Locate every blood parasite and identify its species.
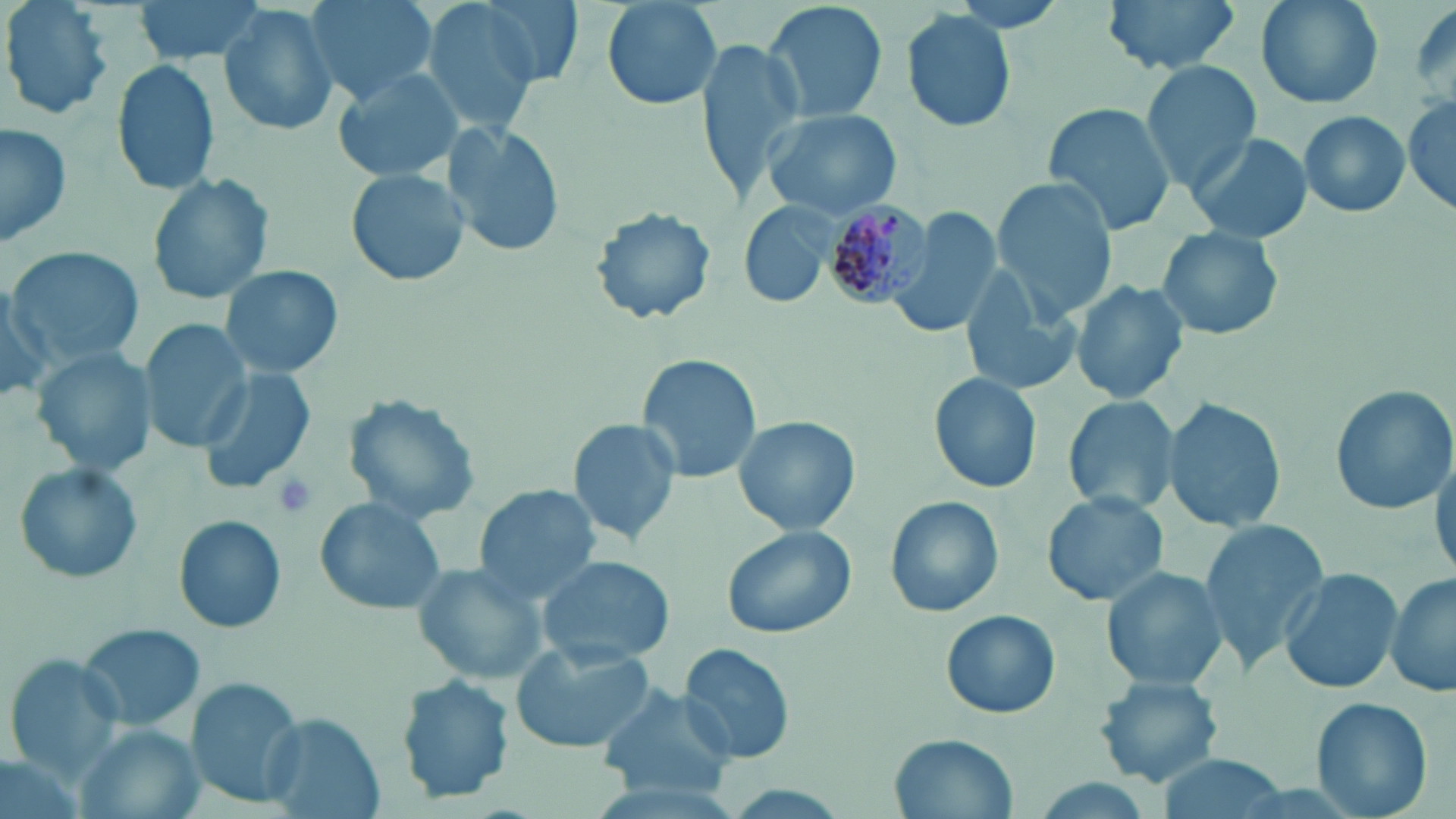

Approximate bounding boxes as [x1, y1, x2, y2] in pixels.
Plasmodium malariae-infected red blood cells: [818, 198, 933, 308].
No Plasmodium falciparum, Plasmodium ovale, Plasmodium vivax, Babesia divergens, or Trypanosoma brucei observed.

Uninfected red blood cell locations: [2, 0, 112, 125], [136, 0, 267, 65], [305, 0, 440, 105], [420, 0, 557, 134], [471, 0, 586, 89], [599, 0, 724, 111], [763, 0, 887, 126], [1102, 0, 1243, 76], [1251, 0, 1385, 112], [218, 6, 341, 138], [902, 12, 1017, 132], [695, 36, 805, 201], [1140, 60, 1264, 190], [112, 61, 220, 194], [332, 69, 465, 185], [1402, 94, 1455, 221], [1044, 100, 1178, 237], [1296, 109, 1412, 218], [764, 110, 900, 218], [442, 121, 566, 258], [0, 122, 75, 249], [1187, 131, 1314, 243], [345, 168, 470, 289], [147, 171, 274, 306], [992, 176, 1118, 321], [737, 201, 838, 310], [588, 203, 719, 327], [885, 209, 1002, 339], [1157, 226, 1286, 340], [3, 244, 147, 368], [220, 264, 341, 379], [959, 270, 1083, 400], [0, 279, 52, 405], [1070, 283, 1188, 405], [141, 320, 252, 450], [33, 347, 156, 477], [639, 354, 766, 485], [198, 364, 319, 493], [929, 373, 1043, 495], [1329, 383, 1454, 514], [342, 393, 483, 520], [1062, 395, 1181, 516], [1162, 395, 1289, 536], [731, 414, 860, 535], [569, 418, 682, 546], [1431, 444, 1455, 582], [11, 461, 146, 587], [473, 484, 600, 604], [1042, 491, 1169, 607], [884, 494, 1005, 619], [313, 497, 447, 614], [172, 514, 288, 634], [1199, 517, 1331, 670], [722, 524, 859, 638], [538, 557, 677, 663], [410, 560, 548, 685], [1101, 565, 1229, 692], [1279, 566, 1401, 694], [1386, 573, 1454, 700], [941, 611, 1061, 720], [78, 621, 206, 732], [509, 641, 656, 755], [678, 641, 798, 764], [3, 656, 123, 778], [1093, 672, 1225, 788], [398, 676, 514, 803], [185, 679, 307, 806], [598, 687, 732, 799], [1311, 697, 1432, 818], [258, 713, 383, 817], [80, 726, 200, 819], [889, 732, 1016, 817], [1156, 755, 1289, 819]. Platelet locations: [271, 472, 319, 520]. Slide-level diagnosis: Plasmodium malariae. Light microscopy. Thin blood film. Single field of view. 1000x magnification. Image is 1456×819 pixels. May-Grünwald-Giemsa-stained preparation.